Comment on the morphology of the erythrocytes.
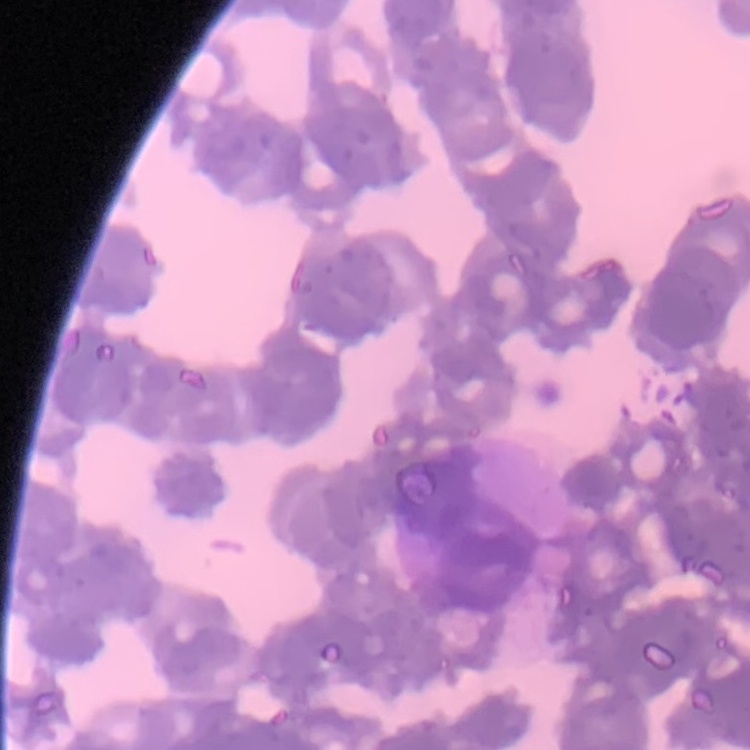
Rouleaux formation.

Thin blood film. Stained with either Field's or Giemsa. One tile cut from a larger photomicrograph.